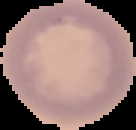

{
  "preparation": "thin blood smear",
  "image_type": "segmented cell region with the area outside set to black",
  "image_size": "136×130 pixels",
  "malaria_status": "uninfected"
}